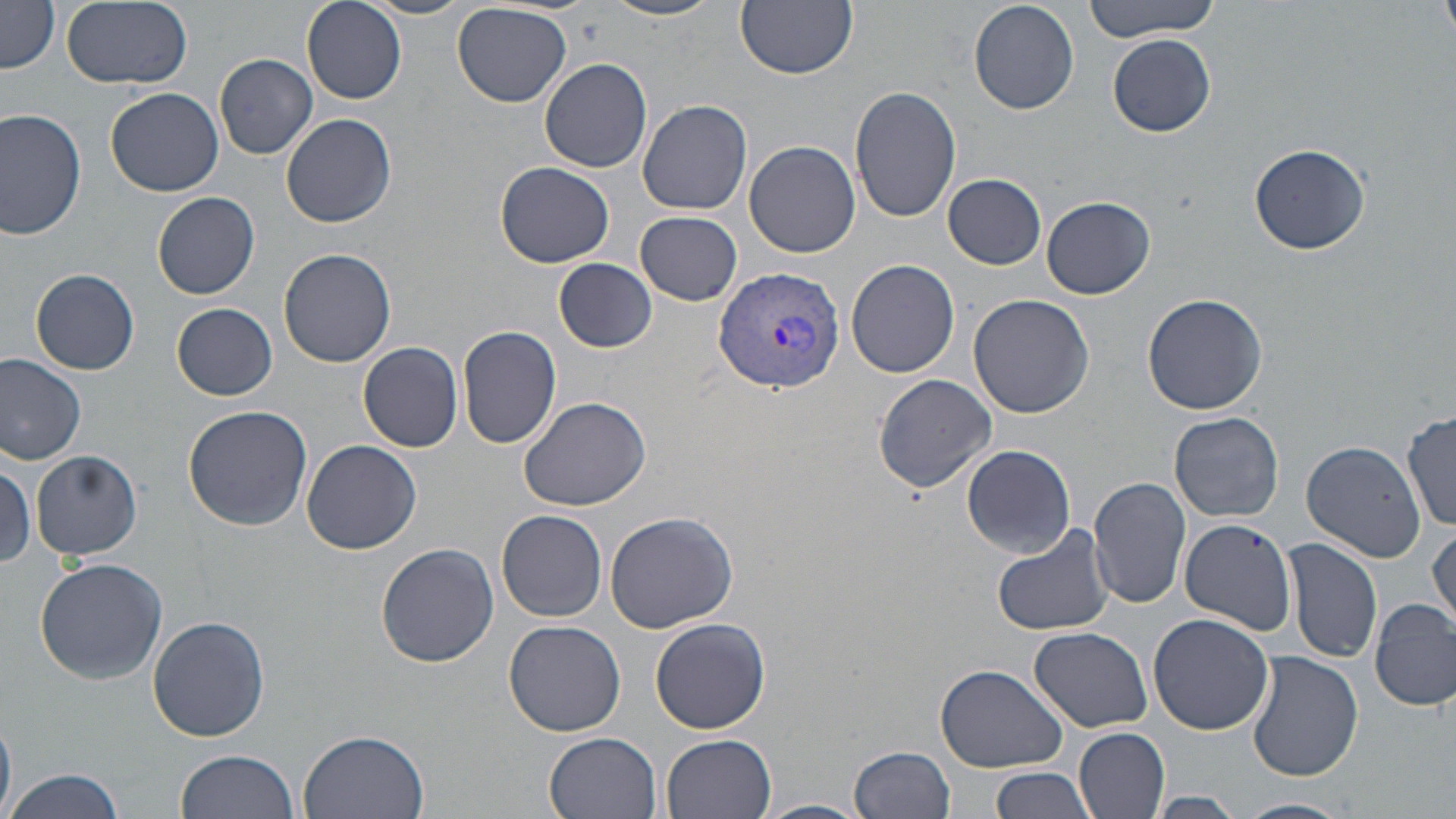
Approximate bounding boxes as (x1,y1)-(x2,y2) corner pairs in pixels. Plasmodium vivax-infected red blood cell locations: (713,264)-(845,393). Uninfected red blood cell locations: (361,0)-(478,19), (604,0)-(724,22), (735,0)-(858,78), (1087,0)-(1221,42), (1439,0)-(1456,42), (61,1)-(192,89), (302,1)-(406,103), (969,1)-(1079,115), (1,3)-(61,72), (453,3)-(571,108), (1109,35)-(1215,136), (216,53)-(317,159), (539,58)-(652,172), (850,86)-(961,223), (107,88)-(224,197), (637,98)-(752,215), (0,107)-(89,240), (281,112)-(397,227), (745,140)-(861,258), (1248,142)-(1369,255), (496,162)-(614,268), (943,173)-(1047,268), (153,192)-(259,300), (1041,196)-(1155,300), (636,210)-(742,305), (279,249)-(396,366), (554,259)-(657,352), (847,259)-(959,378), (31,268)-(141,374), (1142,291)-(1269,415), (967,294)-(1094,419), (172,303)-(279,401), (458,324)-(563,449), (359,341)-(463,452), (0,355)-(87,464), (873,373)-(996,494), (517,394)-(652,512), (183,405)-(314,532), (1169,412)-(1283,522), (1404,412)-(1456,533), (300,438)-(423,555), (1301,440)-(1426,562), (962,444)-(1075,558), (30,449)-(143,562), (0,459)-(37,569), (1090,475)-(1193,609), (497,511)-(608,622), (604,512)-(738,633), (1179,518)-(1297,634), (992,523)-(1116,638), (1428,525)-(1455,631), (1283,538)-(1382,665), (376,541)-(499,668), (34,557)-(168,684), (1370,598)-(1455,711), (148,613)-(272,741), (1148,613)-(1275,735), (650,616)-(772,734), (504,619)-(626,736), (1031,626)-(1153,732), (1247,651)-(1363,781), (936,663)-(1068,773), (1075,726)-(1171,819), (298,730)-(431,819), (545,732)-(661,818), (663,733)-(778,818), (850,745)-(957,819), (177,749)-(303,818), (987,765)-(1097,819), (3,768)-(126,819), (1146,792)-(1246,818), (1234,797)-(1354,819), (753,799)-(870,819). Slide-level diagnosis: Plasmodium vivax. May-Grünwald-Giemsa stain. Thin blood film. One field of a larger specimen. Optical microscopy. Captured at 1000x magnification. Image is 1456×819 pixels.